Give the position of every Plasmodium parasite visible.
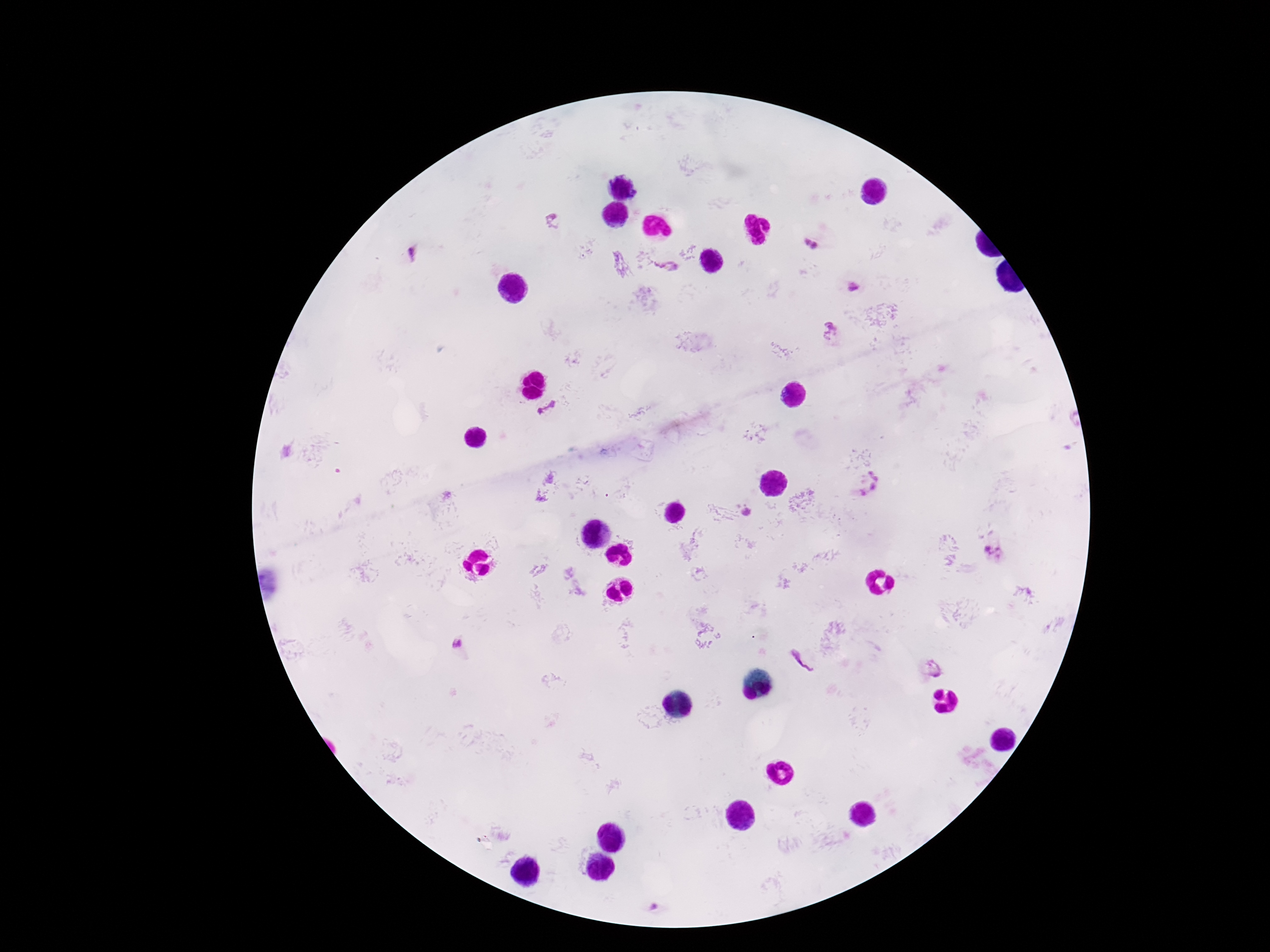
Approximate centers as [x, y] in pixels.
Plasmodium parasites: [553, 222], [805, 241], [815, 246], [413, 256], [669, 267], [855, 288], [829, 331], [550, 411], [869, 484], [746, 513], [995, 553], [459, 643], [803, 661], [932, 668], [654, 908].

Smartphone photograph taken through the microscope eyepiece. Thick blood film. Patient malaria status: positive. Giemsa stain. 100x magnification. One field from this slide. Image is 1270×952 pixels.